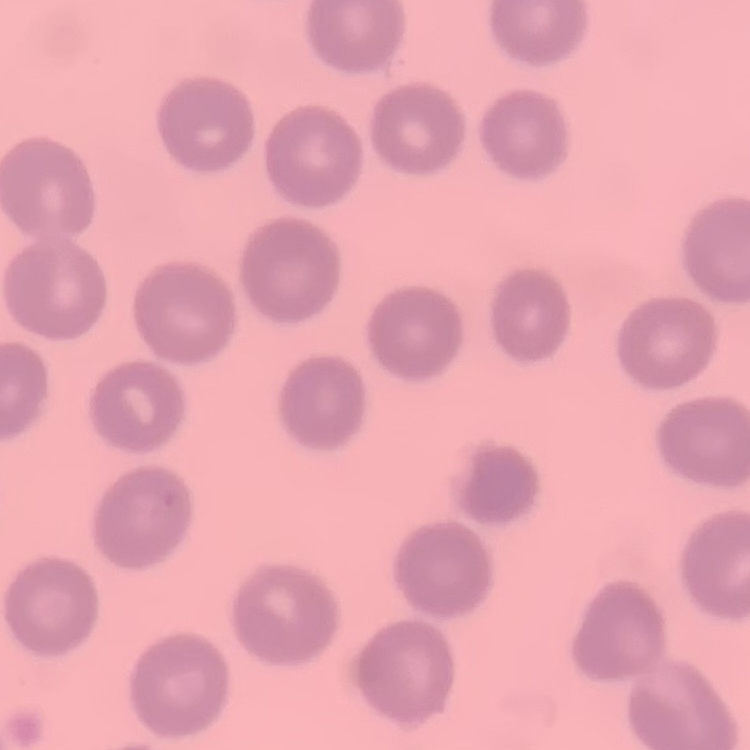

Summary:
  - Red blood cell morphology: no rouleaux formation
  - Preparation: thin blood smear
  - Image type: one tile cut from a larger photomicrograph
  - Stain: Field's or Giemsa